Identify the blood parasite species.
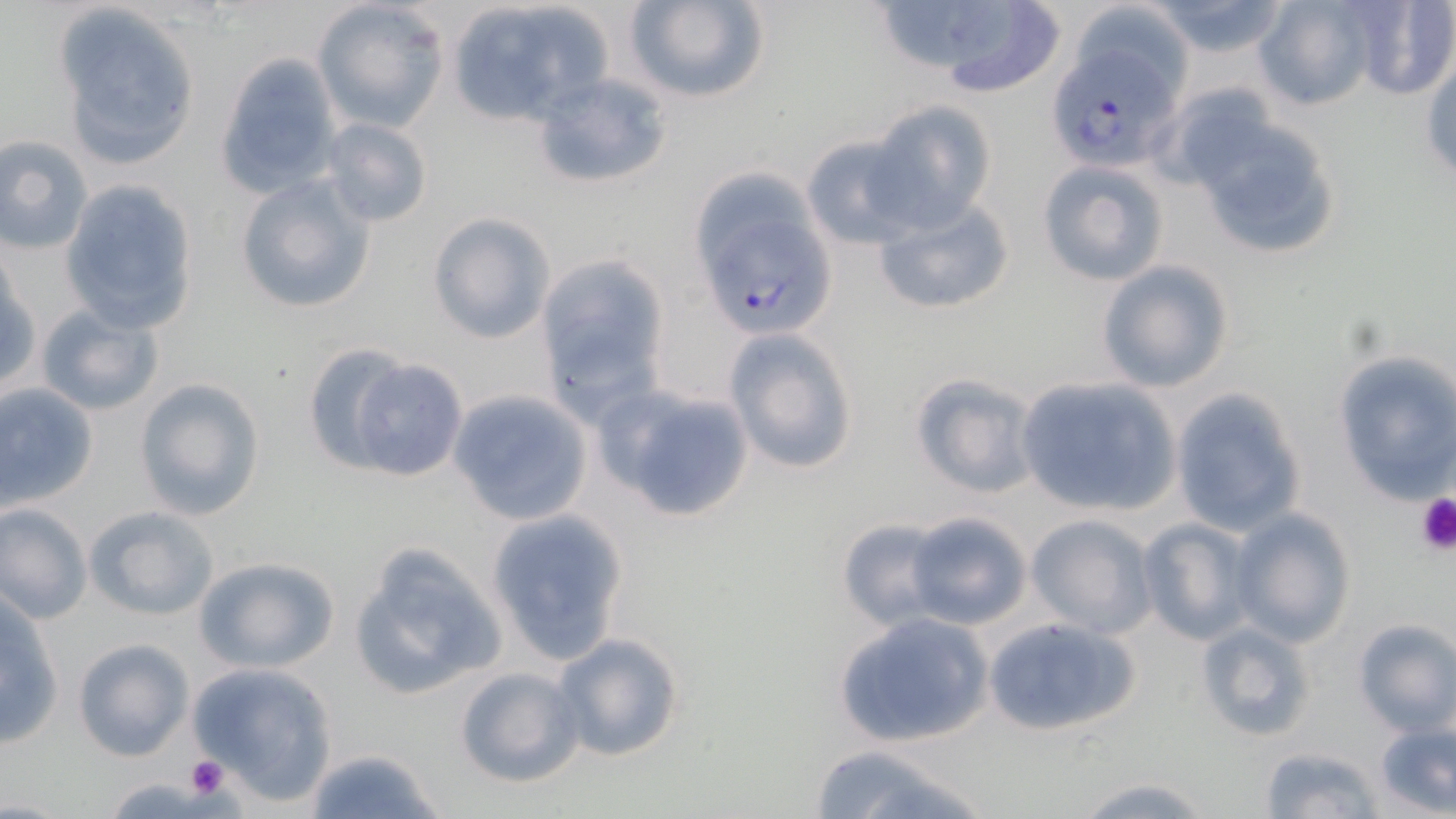
Plasmodium falciparum.

magnification = 1000x
Plasmodium falciparum-infected red blood cell locations = approximate bounding boxes as (x1,y1)-(x2,y2) corner pairs in pixels: (1045,43)-(1183,176), (699,163)-(845,331)
stain = May-Grünwald-Giemsa
image size = 1456×819 pixels
modality = light microscopy
field of view = one of a larger specimen
uninfected red blood cell locations = approximate bounding boxes as (x1,y1)-(x2,y2) corner pairs in pixels: (311,0)-(448,131), (621,0)-(772,106), (871,0)-(1068,97), (1143,0)-(1297,59), (1252,0)-(1381,111), (1342,0)-(1456,101), (444,2)-(610,126), (56,8)-(199,165), (1421,51)-(1456,187), (215,53)-(344,196), (865,101)-(996,233), (1182,107)-(1345,265), (318,117)-(433,228), (801,131)-(918,250), (0,134)-(94,254), (1035,160)-(1170,287), (234,174)-(377,314), (60,183)-(198,349), (871,196)-(1013,316), (428,212)-(554,344), (535,257)-(670,415), (1096,259)-(1235,394), (34,302)-(164,418), (725,327)-(860,474), (299,342)-(410,471), (1331,348)-(1456,502), (346,357)-(468,482), (908,371)-(1041,498), (135,377)-(266,521), (1013,377)-(1182,519), (0,381)-(100,510), (594,383)-(757,523), (1169,386)-(1306,537), (450,388)-(594,526), (0,503)-(93,625), (86,505)-(222,622), (1228,507)-(1357,647), (487,511)-(628,667), (906,511)-(1032,630), (1027,513)-(1158,639), (837,518)-(948,630), (1136,518)-(1257,645), (348,543)-(508,705), (193,556)-(339,672), (0,593)-(65,749), (836,610)-(997,748), (983,615)-(1142,739), (1352,617)-(1456,736), (1195,620)-(1318,743), (549,630)-(687,762), (72,637)-(193,761), (187,662)-(340,804), (453,666)-(584,788), (1374,724)-(1456,816), (802,744)-(995,819), (1258,746)-(1383,819), (304,747)-(445,819), (1071,773)-(1217,818)
preparation = thin blood smear
platelet locations = approximate bounding boxes as (x1,y1)-(x2,y2) corner pairs in pixels: (1413,492)-(1456,556), (185,756)-(228,798)